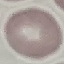
result = negative for malaria parasites
stain = Giemsa
image type = cell patch, automatically extracted from a larger field of view and resized to 64 × 64 pixels
capture = smartphone through the microscope eyepiece
preparation = thin blood smear